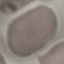 Malaria status: uninfected. Photographed with a smartphone camera at the microscope eyepiece. Thin blood smear. Giemsa-stained preparation. Automatically extracted cell patch, resized to 64 × 64 pixels.